Locate every blood parasite and identify its species.
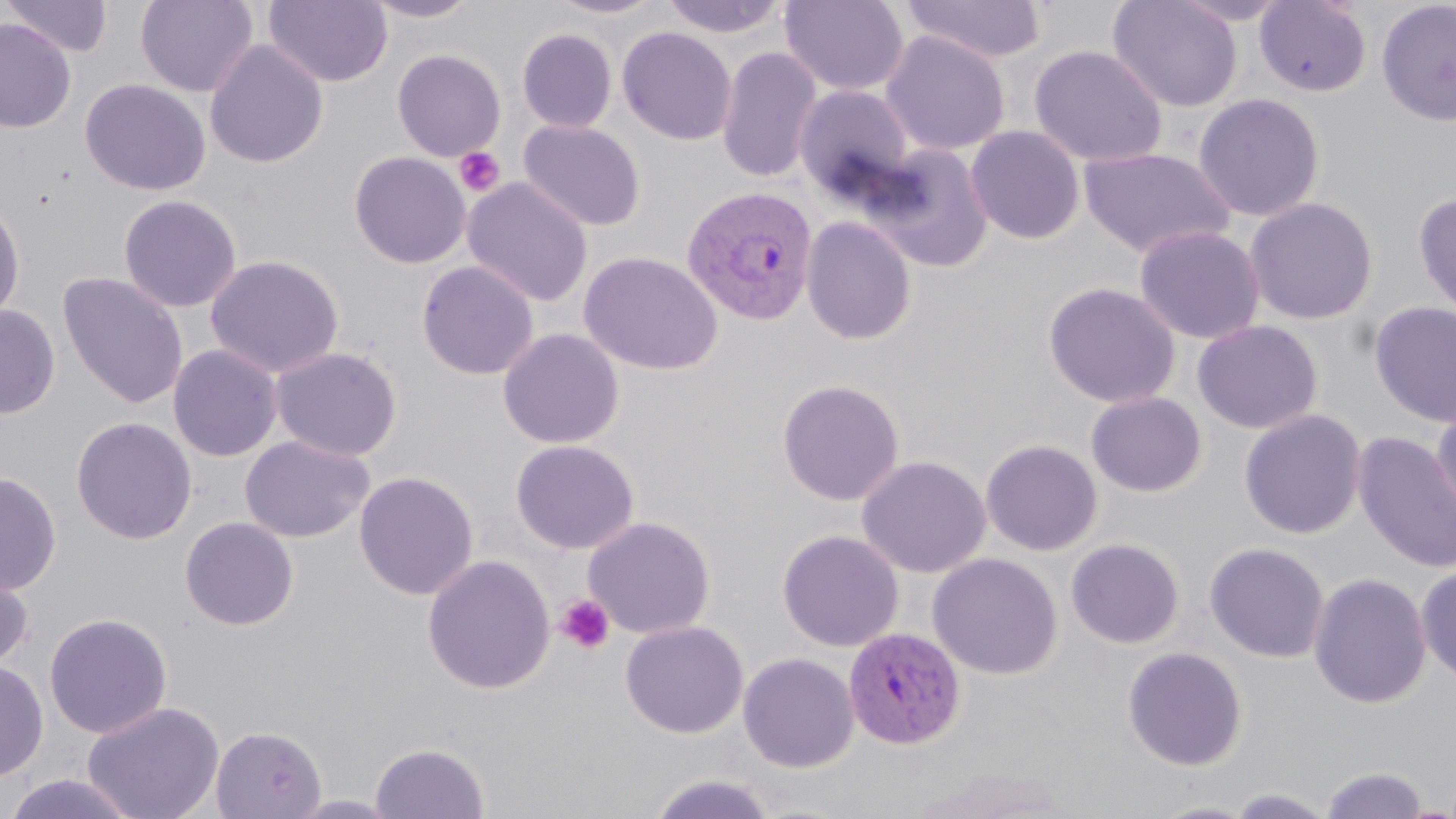
Approximate bounding boxes as (x1, y1, x2, y2) in pixels.
Plasmodium vivax-infected red blood cells: (681, 184, 819, 326), (843, 626, 965, 749).
No Plasmodium falciparum, Plasmodium ovale, Plasmodium malariae, Babesia divergens, or Trypanosoma brucei observed.

slide_level_diagnosis: Plasmodium vivax
modality: optical microscopy
uninfected_red_blood_cell_locations: 'approximate bounding boxes as (x1, y1, x2, y2) in pixels: (3, 0, 115, 58), (135, 0, 258, 97), (263, 0, 393, 87), (361, 0, 483, 23), (547, 0, 667, 20), (660, 0, 790, 39), (780, 0, 909, 96), (900, 0, 1047, 64), (1107, 0, 1244, 112), (1254, 0, 1372, 97), (1376, 1, 1456, 127), (0, 18, 76, 133), (616, 26, 738, 145), (517, 28, 618, 133), (880, 30, 1011, 156), (204, 39, 329, 168), (1028, 44, 1168, 168), (715, 45, 824, 183), (392, 49, 506, 161), (79, 78, 211, 196), (793, 84, 916, 201), (1192, 92, 1325, 222), (518, 119, 646, 231), (965, 125, 1086, 244), (866, 143, 995, 272), (1078, 146, 1235, 259), (349, 151, 471, 269), (462, 177, 594, 307), (1414, 190, 1456, 323), (118, 194, 242, 313), (1244, 196, 1379, 325), (0, 199, 26, 326), (801, 215, 918, 345), (1133, 224, 1266, 345), (579, 251, 725, 376), (204, 254, 345, 378), (416, 260, 539, 380), (57, 271, 189, 410), (1042, 281, 1181, 408), (1369, 300, 1456, 428), (0, 304, 60, 419), (1192, 319, 1323, 434), (496, 327, 625, 449), (167, 343, 284, 462), (270, 346, 403, 462), (776, 378, 905, 506), (1085, 391, 1207, 497), (1430, 401, 1456, 528), (1239, 408, 1367, 539), (71, 416, 197, 545), (1352, 431, 1456, 574), (239, 434, 375, 543), (510, 439, 640, 555), (980, 439, 1103, 556), (855, 454, 992, 578), (354, 470, 479, 600), (0, 471, 62, 596), (582, 515, 716, 639), (179, 516, 299, 630), (777, 528, 904, 652), (1066, 538, 1184, 648), (1204, 542, 1330, 663), (927, 552, 1064, 679), (421, 554, 557, 694), (0, 556, 35, 675), (1415, 565, 1456, 683), (1308, 571, 1432, 709), (43, 612, 173, 738), (620, 620, 749, 738), (1121, 645, 1248, 771), (738, 651, 860, 772), (0, 659, 49, 782), (82, 700, 225, 819), (209, 724, 327, 819), (370, 741, 491, 818), (913, 765, 1076, 818), (1320, 765, 1431, 818), (4, 772, 140, 819), (647, 772, 778, 819), (1226, 787, 1338, 818), (1144, 799, 1263, 819)'
stain: May-Grünwald-Giemsa
preparation: thin blood film
image_size: 1456×819 pixels
platelet_locations: 'approximate bounding boxes as (x1, y1, x2, y2) in pixels: (454, 147, 505, 197), (555, 594, 615, 655)'
magnification: 1000x
field_of_view: single